Report the malaria status of this cell.
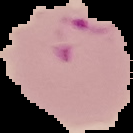

Parasitized.

Image is 133×133 pixels. From a thin blood smear. Segmented cell region on a black background.